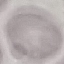

Malaria status: uninfected. Giemsa stain. Acquired by smartphone through the microscope eyepiece. Automatically extracted cell patch, resized to 64 × 64 pixels. Thin blood smear.